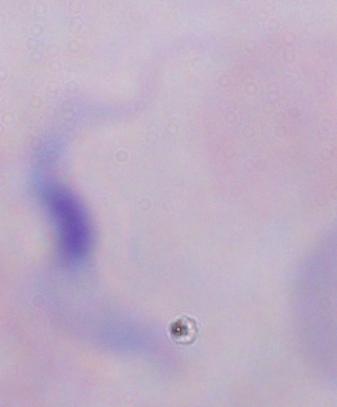
A trypanosome is seen. Captured at 1000x magnification. Photomicrograph.